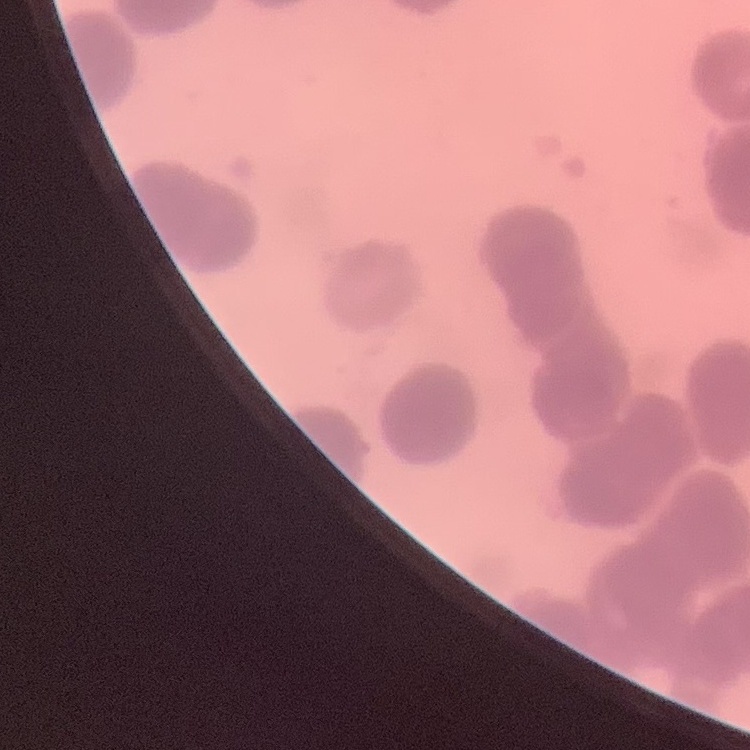

{
  "erythrocyte_morphology": "rouleaux formation",
  "preparation": "thin blood smear",
  "image_type": "square crop of a larger photomicrograph",
  "stain": "Field's or Giemsa"
}